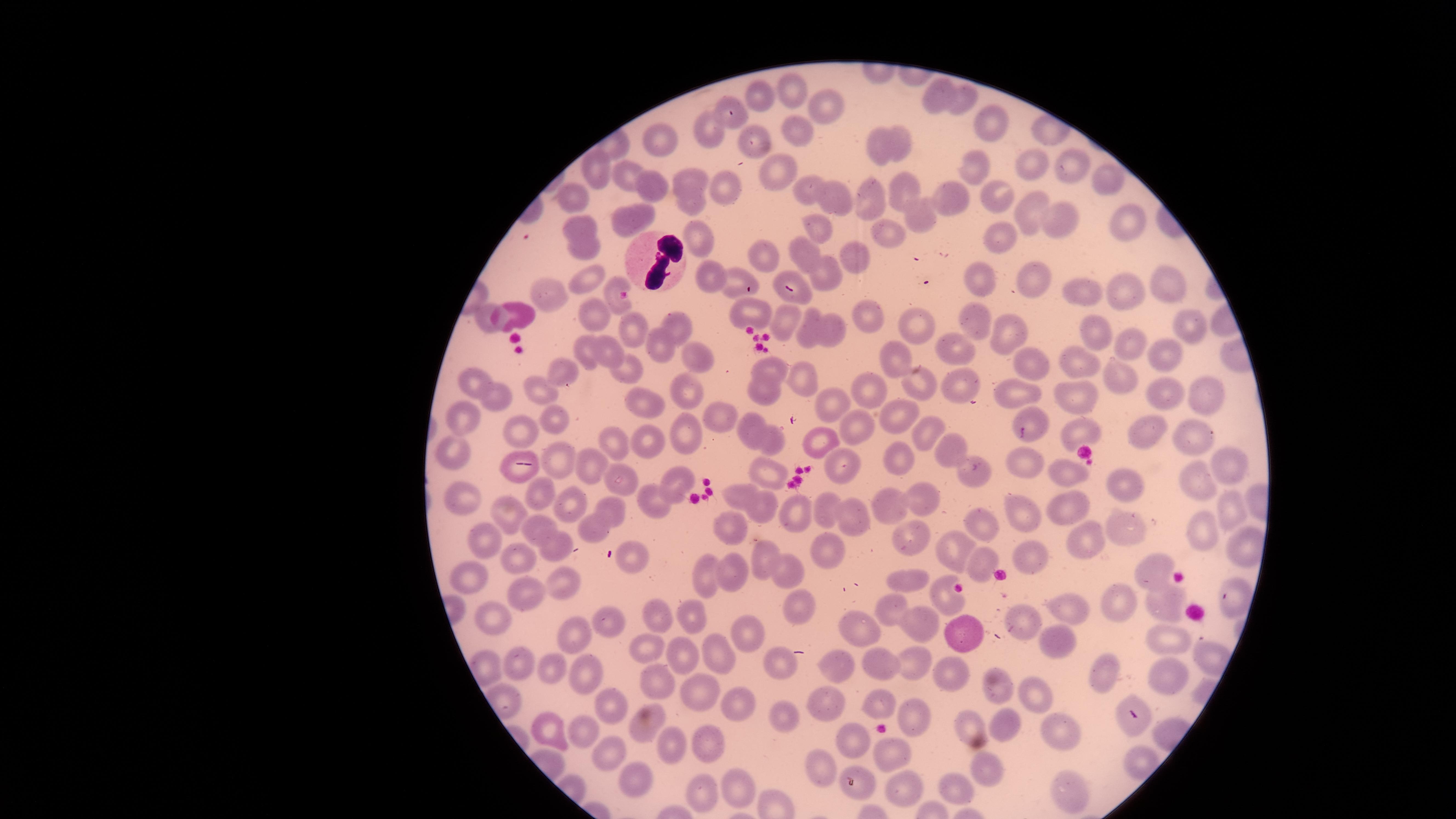
visible_region: circular
presence: no malaria parasites identified
uninfected_RBCs: 'approximate marker points as [x, y] in pixels: [792, 88], [937, 95], [757, 99], [962, 104], [734, 107], [823, 107], [989, 123], [793, 128], [711, 131], [660, 136], [896, 140], [746, 143], [882, 144], [1068, 163], [974, 164], [1035, 169], [782, 174], [597, 176], [627, 176], [684, 178], [1112, 179], [803, 188], [656, 189], [729, 189], [910, 191], [577, 194], [868, 196], [994, 197], [836, 199], [693, 200], [950, 201], [1026, 208], [645, 211], [1065, 214], [921, 219], [1129, 220], [580, 222], [623, 224], [818, 230], [889, 239], [1004, 239], [586, 244], [702, 245], [766, 256], [853, 256], [804, 258], [827, 275], [1029, 277], [708, 278], [1164, 278], [590, 282], [982, 283], [740, 286], [1127, 289], [1086, 290], [559, 293], [609, 293], [796, 295], [751, 307], [516, 315], [482, 316], [872, 316], [595, 317], [924, 321], [784, 323], [980, 323], [1186, 324], [678, 326], [833, 330], [626, 332], [811, 334], [1015, 334], [1096, 336], [952, 346], [606, 347], [658, 348], [1137, 348], [587, 354], [691, 354], [900, 358], [1070, 359], [1164, 361], [1035, 367], [771, 370], [633, 372], [1118, 374], [798, 375], [564, 376], [471, 377], [687, 384], [954, 386], [868, 388], [926, 389], [538, 390], [1159, 390], [1201, 392], [1020, 394], [644, 395], [761, 396], [495, 397], [1077, 399], [834, 401], [717, 414], [890, 414], [1026, 416], [465, 419], [556, 419], [857, 424], [923, 427], [1078, 427], [750, 431], [524, 433], [1150, 434], [684, 435], [1198, 437], [820, 439], [777, 440], [650, 442], [617, 444], [454, 449], [895, 452], [956, 452], [1225, 454], [561, 459], [1013, 459], [848, 463], [597, 466], [979, 468], [1069, 471], [774, 477], [1197, 478], [1128, 482], [617, 484], [675, 485], [739, 491], [543, 494], [462, 499], [924, 499], [571, 504], [605, 504], [649, 505], [893, 505], [1228, 506], [828, 507], [762, 509], [797, 510], [1023, 511], [1079, 511], [505, 513], [852, 518], [734, 522], [1121, 525], [597, 526], [987, 527], [538, 528], [1203, 533], [482, 536], [1079, 536], [914, 543], [957, 548], [563, 550], [825, 553], [1030, 558], [636, 559], [518, 560], [771, 560], [986, 563], [1146, 568], [791, 570], [732, 571], [467, 577], [908, 579], [710, 580], [563, 582], [1235, 590], [943, 593], [523, 594], [795, 595], [1168, 601], [1125, 602], [894, 609], [1078, 611], [695, 617], [1025, 618], [494, 620], [659, 621], [604, 623], [920, 623], [859, 628], [967, 631], [577, 632], [749, 637], [1172, 637], [1055, 643], [649, 648], [721, 656], [681, 659], [911, 662], [779, 663], [839, 665], [882, 665], [519, 666], [589, 669], [949, 669], [551, 675], [1106, 676], [1164, 677], [655, 678], [998, 688], [691, 691], [1031, 693], [825, 703], [876, 703], [613, 706], [732, 707], [917, 714], [786, 718], [1009, 723], [586, 725], [971, 725], [1131, 727], [553, 728], [643, 732], [1064, 734], [859, 737], [700, 738], [678, 746], [609, 750], [889, 753], [818, 764], [992, 769], [635, 777], [737, 786], [861, 786], [947, 786], [698, 792], [1074, 792], [908, 793]'
field_of_view: single
capture: smartphone photograph through the microscope eyepiece
stain: Giemsa
WBCs: 'approximate marker points as [x, y] in pixels: [648, 257]'
image_size: 1456×819 pixels
preparation: thin smear of blood